Assess this cell for malaria.
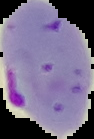
Parasitized.

{
  "image_size": "94×139 pixels",
  "preparation": "thin blood smear",
  "image_type": "cell region segmented out of the field of view; surrounding area masked to black"
}